State which parasite is depicted.
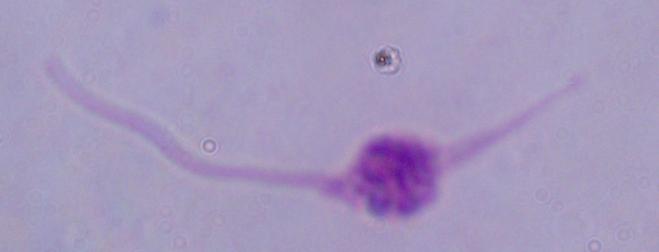

This is Leishmania.

Captured at 1000x magnification. Micrograph.